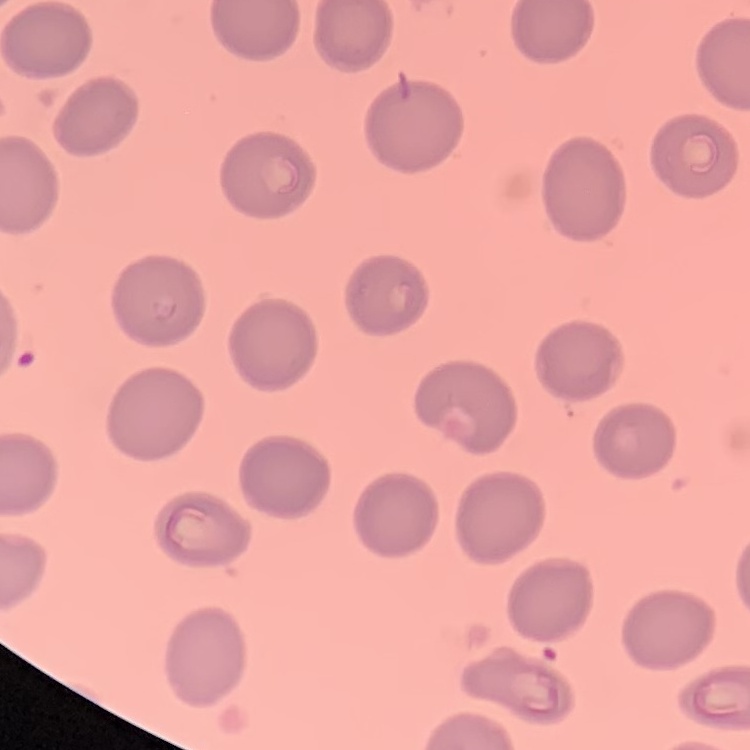
erythrocyte morphology = no rouleaux formation
stain = Field's or Giemsa
preparation = thin blood smear
image type = square crop of a larger photomicrograph